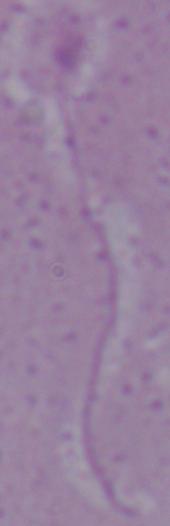
Summary:
  - Magnification: 1000x
  - Modality: micrograph
  - Identification: Leishmania